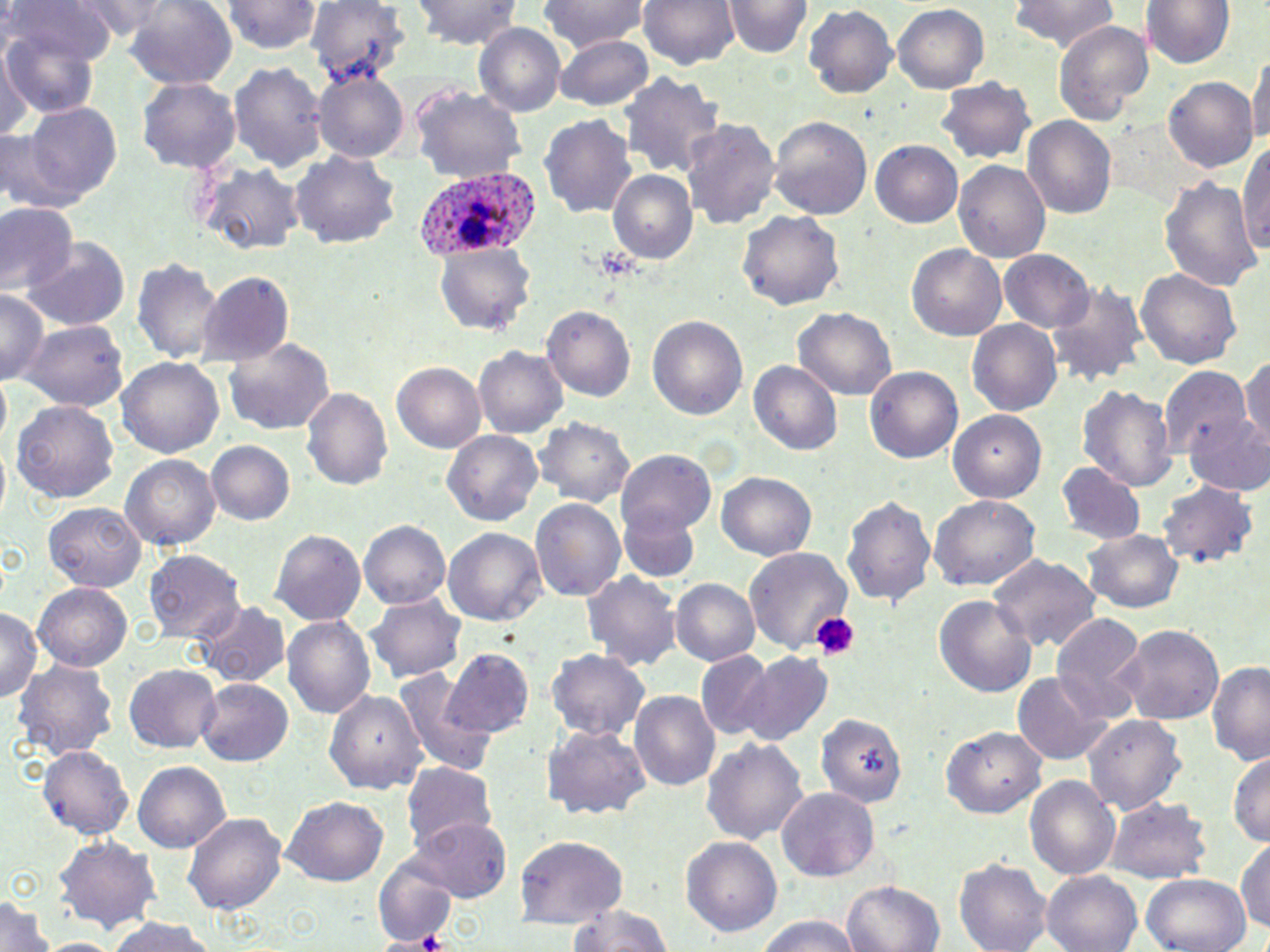

slide-level diagnosis = Plasmodium ovale
image size = 1270×952 pixels
field of view = single
Plasmodium ovale-infected red blood cell locations = approximate bounding boxes as [x1, y1, x2, y2] in pixels: [417, 168, 537, 261]
modality = optical microscopy
magnification = 1000x
platelet locations = approximate bounding boxes as [x1, y1, x2, y2] in pixels: [592, 243, 639, 280], [809, 613, 862, 662], [414, 929, 453, 951]
stain = May-Grünwald-Giemsa
preparation = thin blood film
uninfected red blood cell locations = approximate bounding boxes as [x1, y1, x2, y2] in pixels: [7, 0, 112, 76], [73, 0, 182, 39], [125, 0, 238, 93], [226, 0, 323, 52], [414, 0, 524, 48], [540, 0, 648, 50], [638, 0, 740, 69], [1007, 0, 1124, 57], [1144, 0, 1233, 71], [725, 1, 810, 58], [307, 2, 407, 84], [803, 6, 898, 98], [891, 6, 990, 93], [1054, 20, 1154, 129], [474, 24, 566, 118], [4, 26, 103, 118], [555, 35, 656, 109], [1, 46, 25, 141], [1249, 49, 1270, 156], [227, 60, 326, 171], [314, 70, 410, 162], [622, 72, 724, 182], [934, 76, 1036, 167], [137, 77, 241, 175], [1165, 77, 1259, 173], [412, 81, 526, 187], [21, 103, 122, 208], [542, 114, 638, 221], [769, 115, 873, 223], [1024, 116, 1117, 222], [684, 119, 776, 231], [1242, 133, 1270, 266], [869, 140, 964, 227], [292, 150, 400, 251], [954, 160, 1051, 262], [192, 161, 304, 254], [610, 170, 698, 265], [1162, 175, 1261, 297], [1, 204, 77, 295], [738, 207, 843, 311], [23, 240, 129, 331], [435, 243, 537, 339], [908, 245, 1007, 341], [999, 249, 1097, 335], [131, 255, 223, 363], [196, 270, 294, 364], [1136, 270, 1242, 369], [1050, 282, 1146, 386], [0, 288, 48, 389], [796, 306, 895, 400], [544, 307, 635, 400], [646, 315, 748, 421], [968, 320, 1062, 414], [22, 322, 128, 410], [224, 336, 334, 436], [474, 346, 568, 440], [118, 356, 223, 463], [1240, 357, 1270, 449], [751, 361, 843, 457], [391, 362, 485, 452], [866, 365, 964, 464], [1159, 367, 1249, 456], [1077, 382, 1175, 493], [303, 388, 393, 492], [11, 400, 119, 505], [947, 407, 1045, 500], [1184, 410, 1270, 496], [536, 416, 635, 511], [444, 430, 544, 526], [204, 440, 297, 528], [618, 451, 715, 538], [121, 455, 220, 551], [1058, 464, 1146, 545], [718, 472, 816, 562], [1158, 483, 1259, 567], [843, 493, 940, 607], [930, 493, 1041, 592], [530, 499, 626, 606], [44, 503, 146, 593], [619, 508, 697, 584], [359, 520, 451, 609], [272, 527, 368, 625], [444, 528, 546, 626], [1085, 529, 1183, 612], [143, 547, 245, 640], [745, 547, 854, 659], [988, 555, 1102, 656], [583, 571, 677, 672], [671, 578, 760, 668], [35, 582, 133, 670], [934, 594, 1038, 700], [365, 595, 466, 684], [189, 602, 288, 688], [2, 607, 43, 705], [1051, 612, 1147, 724], [283, 616, 375, 717], [1121, 623, 1226, 728], [546, 649, 652, 742], [442, 650, 533, 739], [693, 651, 774, 738], [739, 653, 833, 746], [15, 657, 118, 764], [1206, 661, 1270, 765], [124, 666, 221, 752], [394, 672, 497, 773], [1012, 673, 1112, 764], [198, 679, 292, 767], [327, 688, 426, 795], [629, 691, 720, 792], [817, 712, 905, 808], [1086, 712, 1185, 815], [544, 724, 649, 825], [941, 726, 1045, 819], [702, 736, 809, 846], [40, 745, 133, 841], [1230, 754, 1270, 848], [133, 761, 231, 853], [401, 762, 499, 855], [1024, 773, 1120, 882], [778, 787, 879, 882], [283, 799, 388, 886], [1106, 801, 1212, 883], [185, 812, 287, 917], [414, 820, 511, 900], [515, 835, 627, 926], [1236, 835, 1270, 939], [682, 836, 781, 935], [55, 837, 159, 933], [372, 860, 456, 944], [955, 860, 1051, 951], [1043, 871, 1143, 952], [1143, 873, 1251, 952], [840, 880, 945, 952], [1, 897, 56, 950], [569, 902, 674, 952], [752, 915, 862, 952], [101, 916, 225, 952], [34, 938, 123, 952]